Evaluate for Plasmodium parasites.
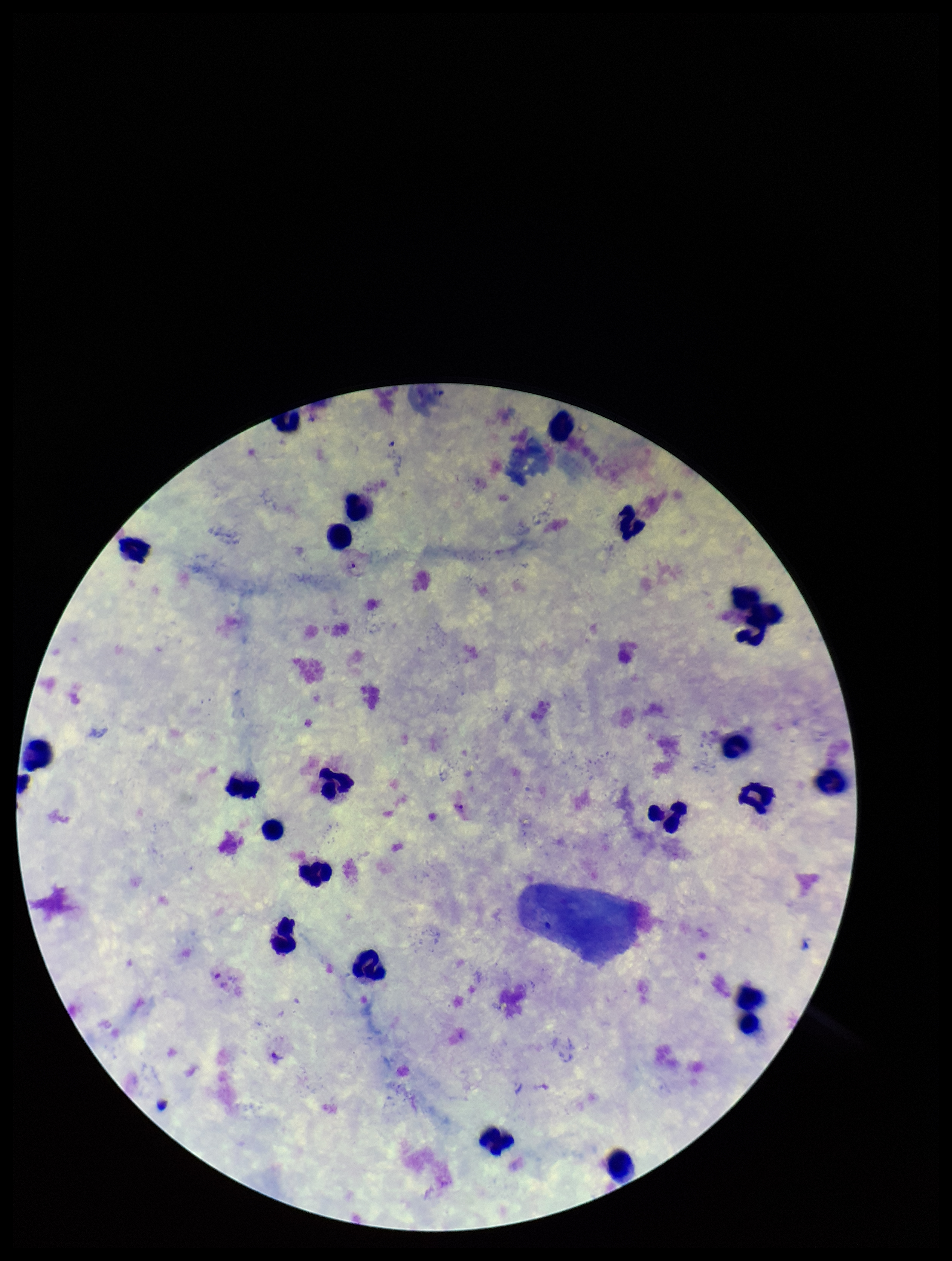
Identified.

Summary:
  - Patient malaria status: infected
  - Species reported for this patient: Plasmodium vivax
  - Stain: Giemsa
  - Parasite count: 3
  - Image size: 952×1261 pixels
  - Capture: smartphone photograph through the microscope eyepiece
  - Field of view: one from this slide
  - Leukocyte count: 23
  - Preparation: thick